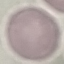
result = no malaria parasites seen
preparation = thin blood smear
image type = cell patch, automatically extracted from a larger field of view and resized to 64 × 64 pixels
capture = smartphone through the microscope eyepiece
stain = Giemsa